Look for Plasmodium parasites.
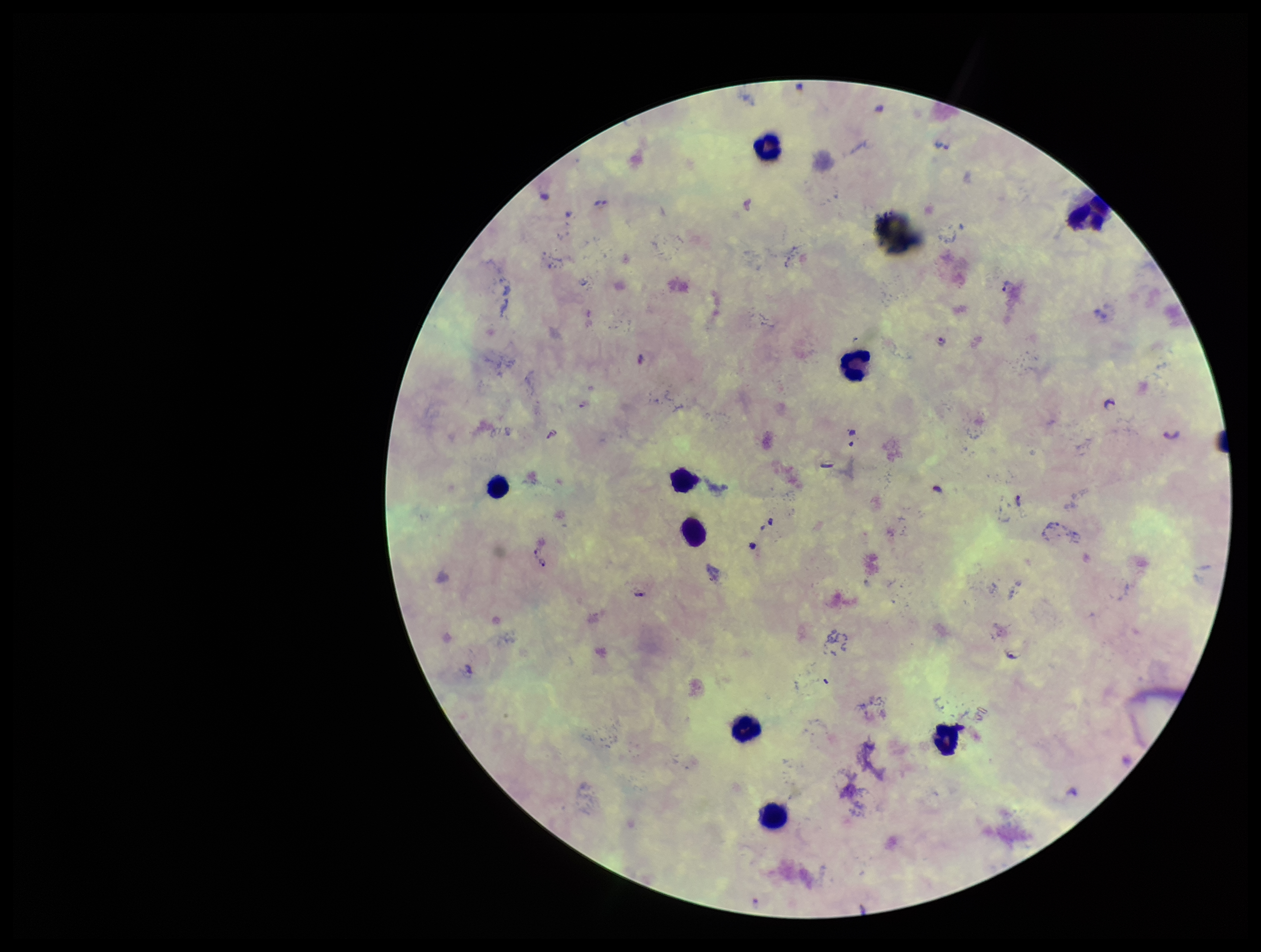
Detected.

Summary:
  - Capture: smartphone photograph through the microscope eyepiece
  - Preparation: thick smear
  - Leukocyte count: 8
  - Parasite count: 2
  - Field of view: one from this slide
  - Patient malaria status: positive
  - Species reported for this patient: Plasmodium falciparum
  - Stain: Giemsa
  - Image size: 1261×952 pixels